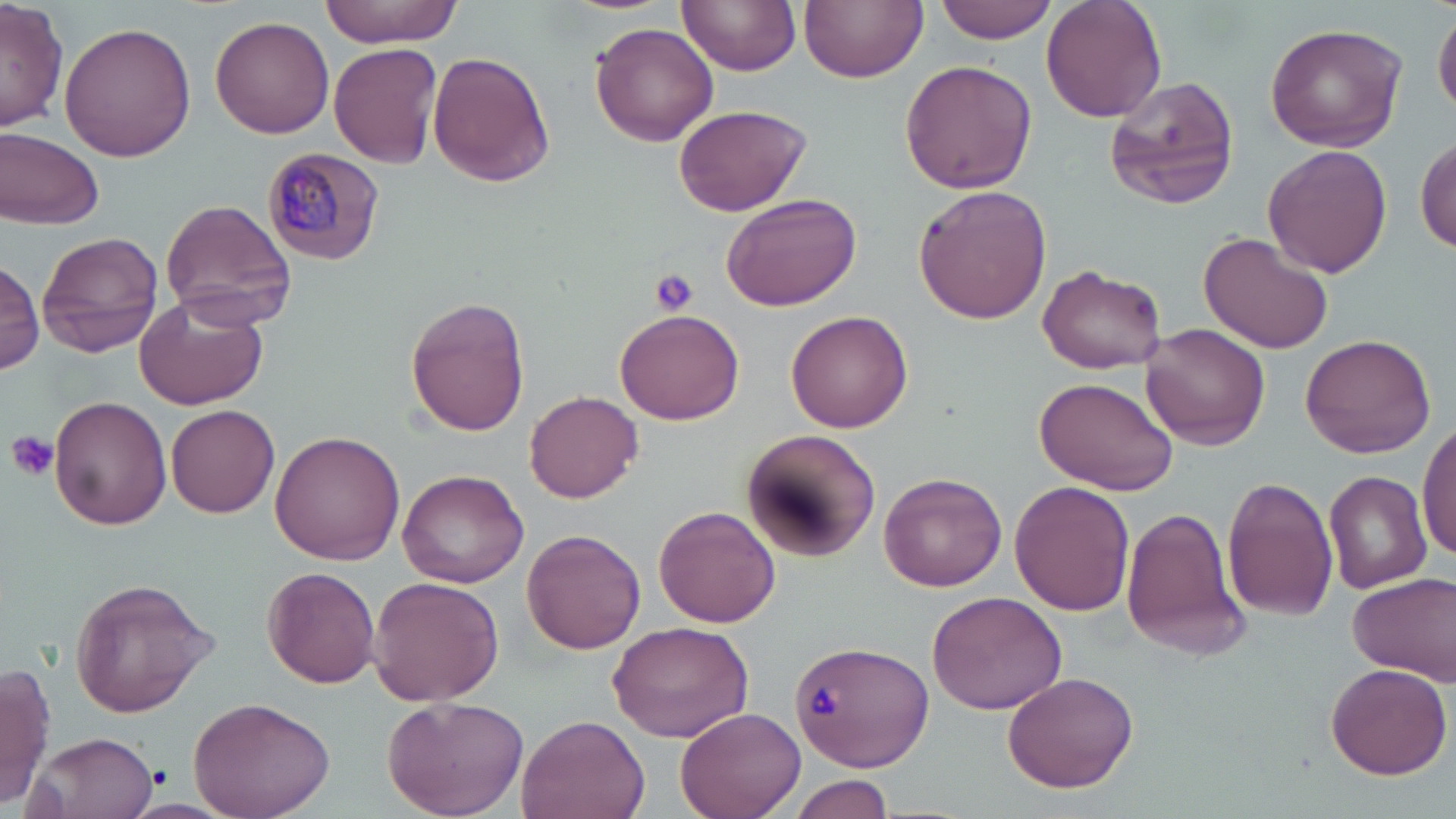
slide-level diagnosis = Plasmodium malariae
modality = light microscopy
magnification = 1000x
field of view = single
preparation = thin blood film
image size = 1456×819 pixels
Plasmodium malariae-infected red blood cell locations = approximate bounding boxes as [x1, y1, x2, y2] in pixels: [263, 147, 386, 265]
stain = May-Grünwald-Giemsa
uninfected red blood cell locations = approximate bounding boxes as [x1, y1, x2, y2] in pixels: [0, 0, 68, 132], [322, 0, 462, 46], [679, 0, 801, 75], [801, 0, 926, 83], [935, 0, 1060, 42], [1040, 0, 1166, 123], [1433, 13, 1455, 118], [209, 15, 335, 139], [60, 20, 196, 162], [589, 21, 719, 147], [1264, 22, 1407, 152], [328, 42, 444, 169], [427, 51, 556, 187], [899, 60, 1038, 195], [1105, 74, 1243, 210], [672, 103, 812, 217], [1, 127, 105, 230], [1415, 134, 1455, 253], [1262, 144, 1392, 280], [912, 185, 1053, 326], [720, 190, 862, 312], [157, 199, 298, 328], [37, 231, 163, 357], [1200, 231, 1334, 353], [0, 259, 45, 374], [1038, 265, 1169, 374], [134, 295, 270, 411], [403, 296, 531, 437], [616, 307, 745, 425], [785, 310, 913, 433], [1141, 324, 1270, 448], [1301, 333, 1437, 459], [1037, 377, 1175, 495], [523, 390, 644, 501], [50, 395, 173, 531], [167, 403, 280, 518], [1417, 417, 1456, 567], [270, 429, 406, 563], [743, 430, 879, 558], [397, 468, 530, 587], [878, 471, 1007, 591], [1324, 471, 1432, 592], [1222, 476, 1340, 621], [1008, 481, 1132, 617], [654, 505, 780, 628], [1121, 507, 1248, 659], [521, 529, 645, 655], [262, 567, 380, 687], [1348, 572, 1455, 681], [367, 575, 505, 706], [67, 576, 218, 717], [929, 589, 1065, 717], [605, 620, 754, 742], [789, 638, 935, 770], [0, 662, 54, 808], [1325, 662, 1453, 781], [1002, 671, 1138, 792], [383, 695, 530, 819], [187, 696, 337, 819], [675, 706, 805, 818], [516, 715, 649, 819], [24, 730, 157, 819], [789, 775, 897, 817]
platelet locations = approximate bounding boxes as [x1, y1, x2, y2] in pixels: [650, 268, 701, 316], [4, 431, 61, 483], [808, 683, 843, 721], [151, 766, 175, 791]